State which parasite is depicted.
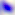

Toxoplasma gondii.

modality = micrograph
magnification = 400x